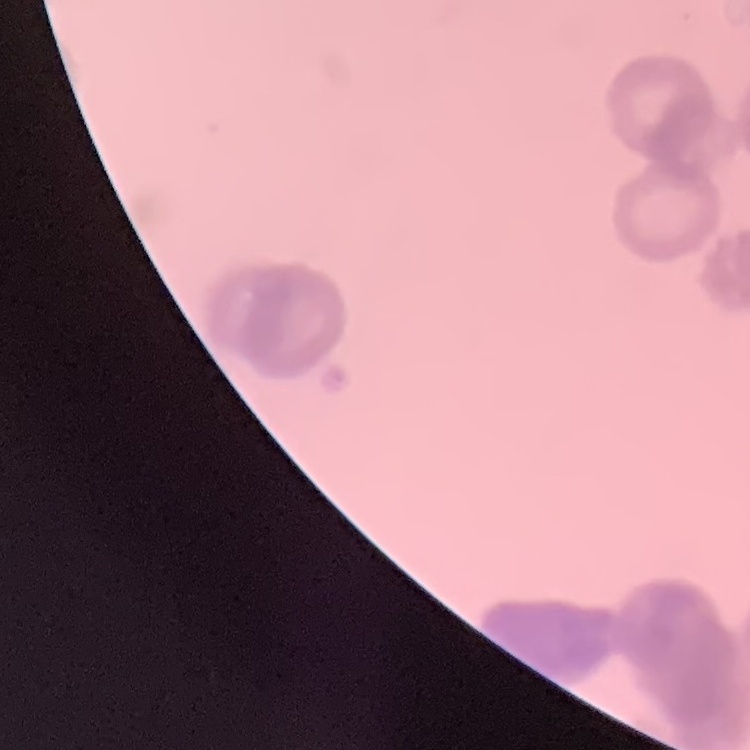
Summary:
  - Red blood cell morphology: rouleaux formation
  - Stain: Field's or Giemsa
  - Preparation: thin blood smear
  - Image type: square crop of a larger photomicrograph